Assess this cell for malaria.
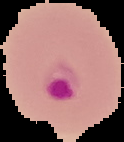
Parasitized.

Summary:
  - Image type: segmented cell region on a black background
  - Preparation: thin blood smear
  - Image size: 124×142 pixels